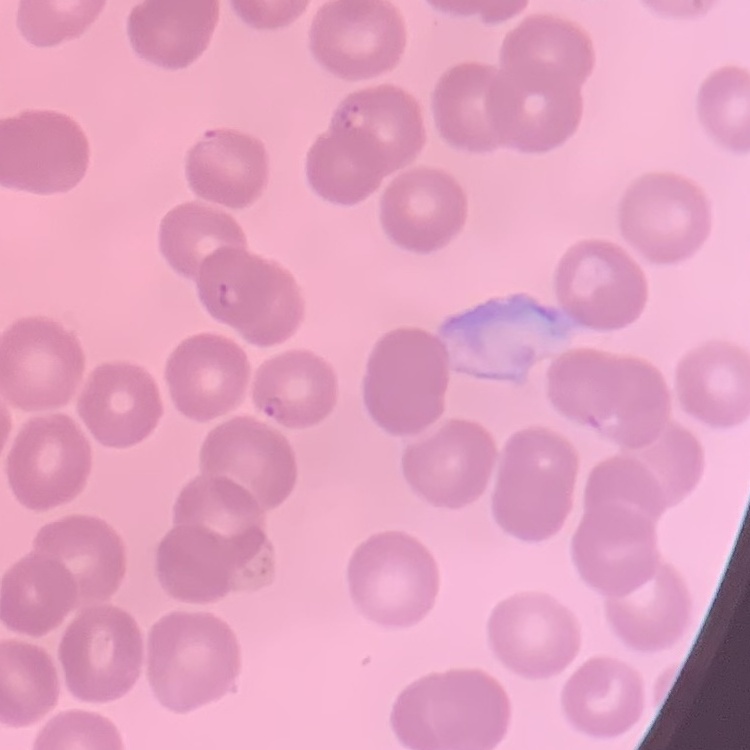
erythrocyte morphology = no rouleaux formation
stain = Field's or Giemsa
preparation = thin peripheral smear
image type = square crop of a larger photomicrograph